Classify this cell by malaria status.
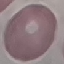
It is uninfected.

Summary:
  - Capture: smartphone through the microscope eyepiece
  - Preparation: thin blood film
  - Stain: Giemsa
  - Image type: automatically extracted cell patch, resized to 64 × 64 pixels